Assess this cell for malaria.
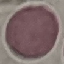

Uninfected.

Cell patch, automatically extracted from a larger field of view and resized to 64 × 64 pixels. Acquired by smartphone through the microscope eyepiece. Giemsa-stained preparation. Thin blood smear.